Classify this cell by malaria status.
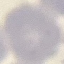

It is uninfected.

Summary:
  - Image type: cell patch, automatically extracted from a larger field of view and resized to 64 × 64 pixels
  - Capture: smartphone camera at the microscope eyepiece
  - Stain: Giemsa
  - Preparation: thin smear